Identify the preparation type.
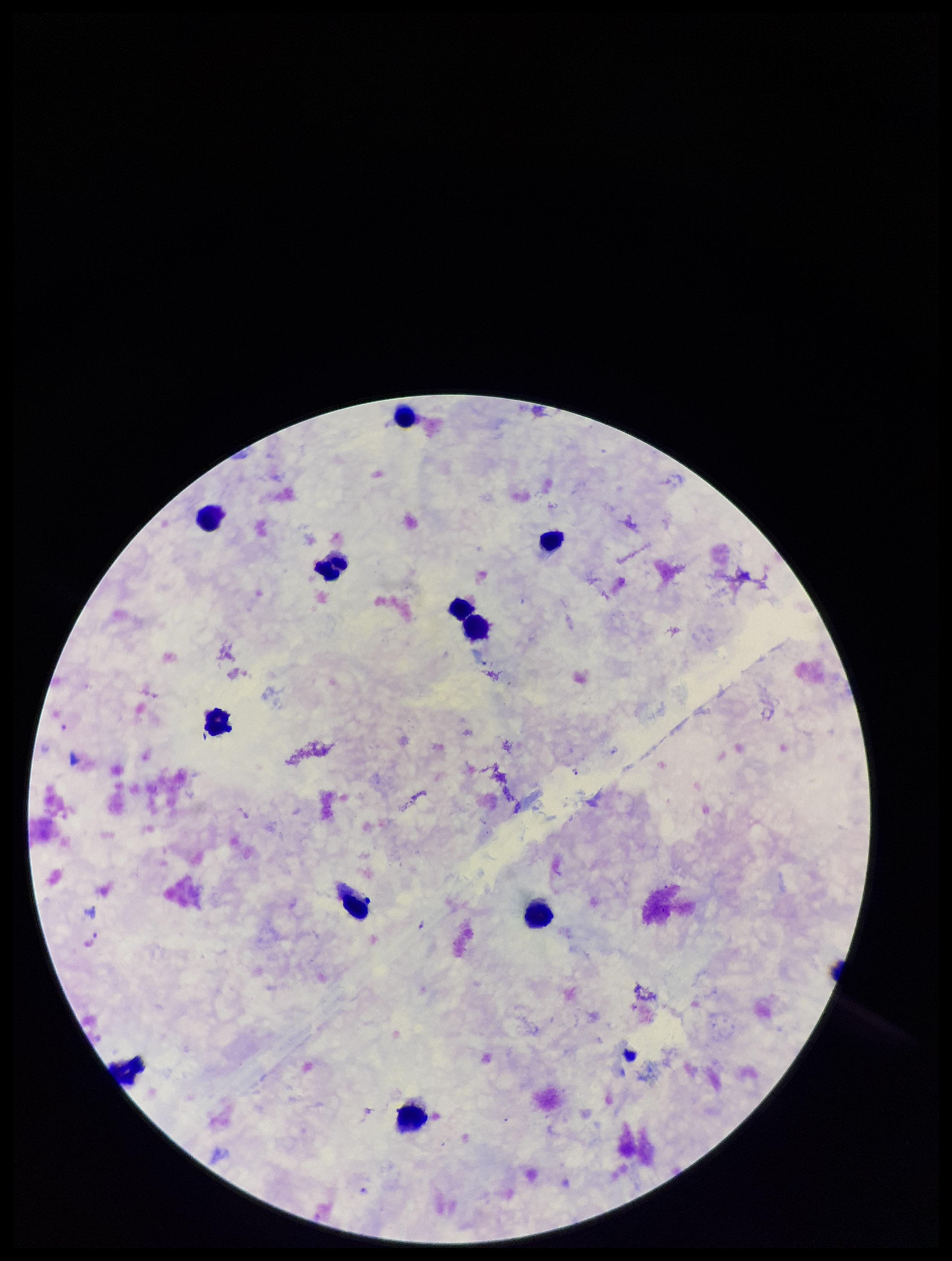

It is a thick blood smear.

image size = 952×1261 pixels
field of view = single
Plasmodium parasites = detected
stain = Giemsa
species reported for this patient = Plasmodium falciparum
leukocyte count = 11
patient malaria status = positive
capture = smartphone photograph through the microscope eyepiece
parasite count = 1